State which cell type is depicted.
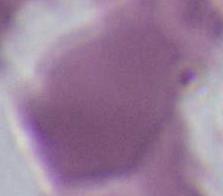

This is an erythrocyte.

Captured at 1000x magnification. Micrograph.